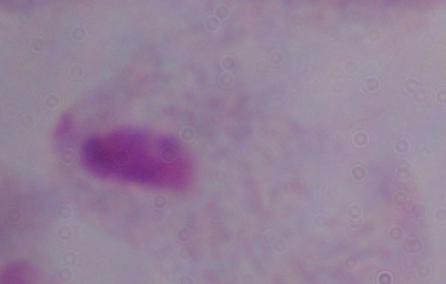

Summary:
  - Magnification: 1000x
  - Identification: trichomonad
  - Modality: micrograph